Assess this cell for malaria.
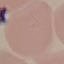
It is uninfected.

preparation = thin smear
stain = Giemsa
image type = automatically extracted cell patch, resized to 64 × 64 pixels
capture = smartphone camera at the microscope eyepiece